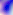 Toxoplasma gondii is seen. Micrograph. 400x magnification.